Give the extent of all Plasmodium malariae-infected red blood cells.
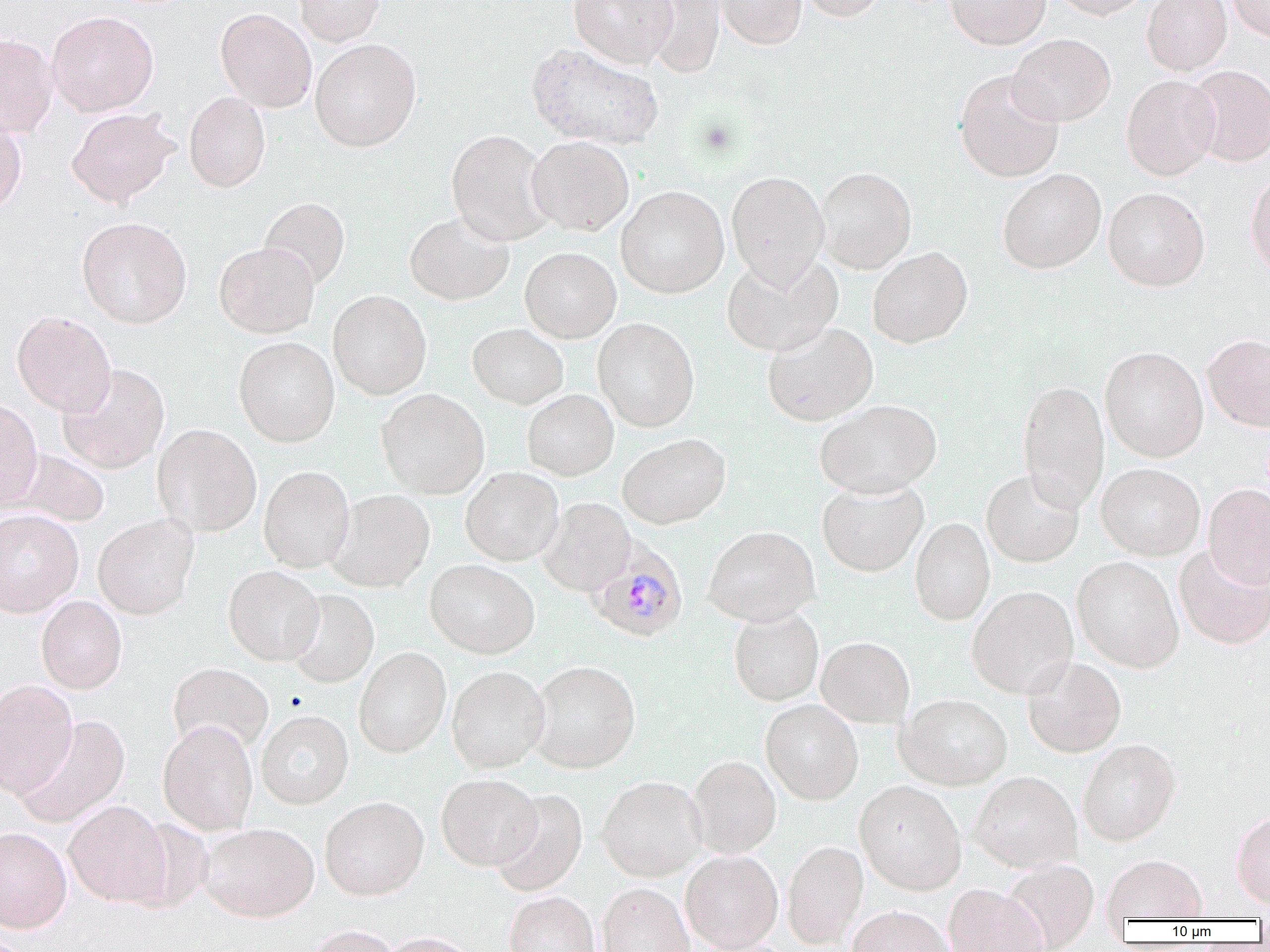

Approximate bounding boxes as [x1, y1, x2, y2] in pixels.
Plasmodium malariae-infected red blood cells: [587, 539, 688, 642].

Uninfected red blood cell locations: [293, 0, 384, 46], [568, 0, 677, 67], [641, 0, 726, 76], [715, 0, 806, 49], [797, 0, 886, 21], [945, 0, 1050, 49], [1051, 0, 1153, 20], [1141, 0, 1231, 75], [1226, 0, 1270, 42], [216, 8, 317, 113], [300, 8, 401, 95], [47, 11, 158, 117], [0, 33, 58, 139], [1007, 34, 1116, 127], [310, 38, 421, 152], [527, 43, 664, 150], [1186, 65, 1270, 167], [954, 71, 1063, 182], [1121, 74, 1221, 180], [184, 92, 271, 192], [66, 107, 179, 207], [0, 111, 27, 215], [446, 129, 554, 246], [527, 136, 634, 236], [815, 167, 916, 273], [997, 168, 1106, 274], [1246, 169, 1270, 279], [726, 171, 829, 285], [616, 185, 730, 298], [1103, 187, 1210, 291], [259, 197, 350, 290], [405, 212, 514, 305], [77, 217, 192, 328], [214, 241, 320, 338], [867, 246, 973, 348], [520, 247, 621, 343], [721, 252, 843, 356], [327, 290, 432, 400], [11, 311, 116, 416], [593, 318, 699, 432], [762, 322, 878, 426], [467, 323, 568, 409], [1203, 333, 1270, 432], [234, 336, 340, 447], [1100, 346, 1209, 462], [57, 363, 170, 473], [1017, 379, 1110, 513], [377, 388, 489, 499], [522, 389, 618, 480], [0, 400, 43, 510], [815, 400, 942, 497], [152, 424, 261, 536], [618, 433, 731, 529], [13, 449, 110, 528], [1096, 463, 1205, 560], [258, 465, 356, 572], [460, 467, 564, 566], [981, 468, 1084, 567], [817, 480, 928, 577], [1203, 484, 1270, 588], [327, 489, 435, 592], [537, 498, 636, 596], [0, 508, 84, 617], [93, 514, 199, 619], [910, 518, 994, 626], [703, 526, 820, 626], [1173, 543, 1270, 650], [1072, 556, 1183, 672], [424, 558, 539, 659], [223, 565, 324, 666], [967, 585, 1078, 698], [285, 589, 379, 688], [36, 595, 127, 694], [728, 607, 824, 706], [816, 636, 914, 727], [354, 647, 451, 757], [1022, 657, 1126, 757], [529, 660, 641, 773], [168, 663, 273, 754], [447, 665, 550, 773], [0, 679, 78, 798], [896, 693, 1012, 790], [761, 699, 863, 805], [256, 710, 354, 809], [13, 715, 130, 828], [158, 720, 258, 835], [1078, 739, 1181, 845], [688, 755, 781, 858], [970, 771, 1082, 873], [436, 773, 541, 870], [596, 775, 706, 881], [854, 780, 966, 894], [491, 789, 588, 897], [320, 796, 429, 900], [64, 800, 171, 907], [1231, 811, 1270, 909], [199, 822, 320, 922], [0, 826, 72, 932], [782, 840, 868, 948], [681, 850, 783, 952], [1103, 855, 1206, 922], [1001, 860, 1099, 951], [597, 883, 694, 952], [943, 884, 1048, 952], [504, 891, 600, 952], [847, 906, 953, 952], [305, 924, 401, 952], [379, 932, 479, 952]. Slide-level diagnosis: Plasmodium malariae. Captured at 1000x magnification. Thin blood smear. Optical microscopy. Image is 1270×952 pixels. Single field of view.